Outline each Plasmodium vivax-infected red blood cell.
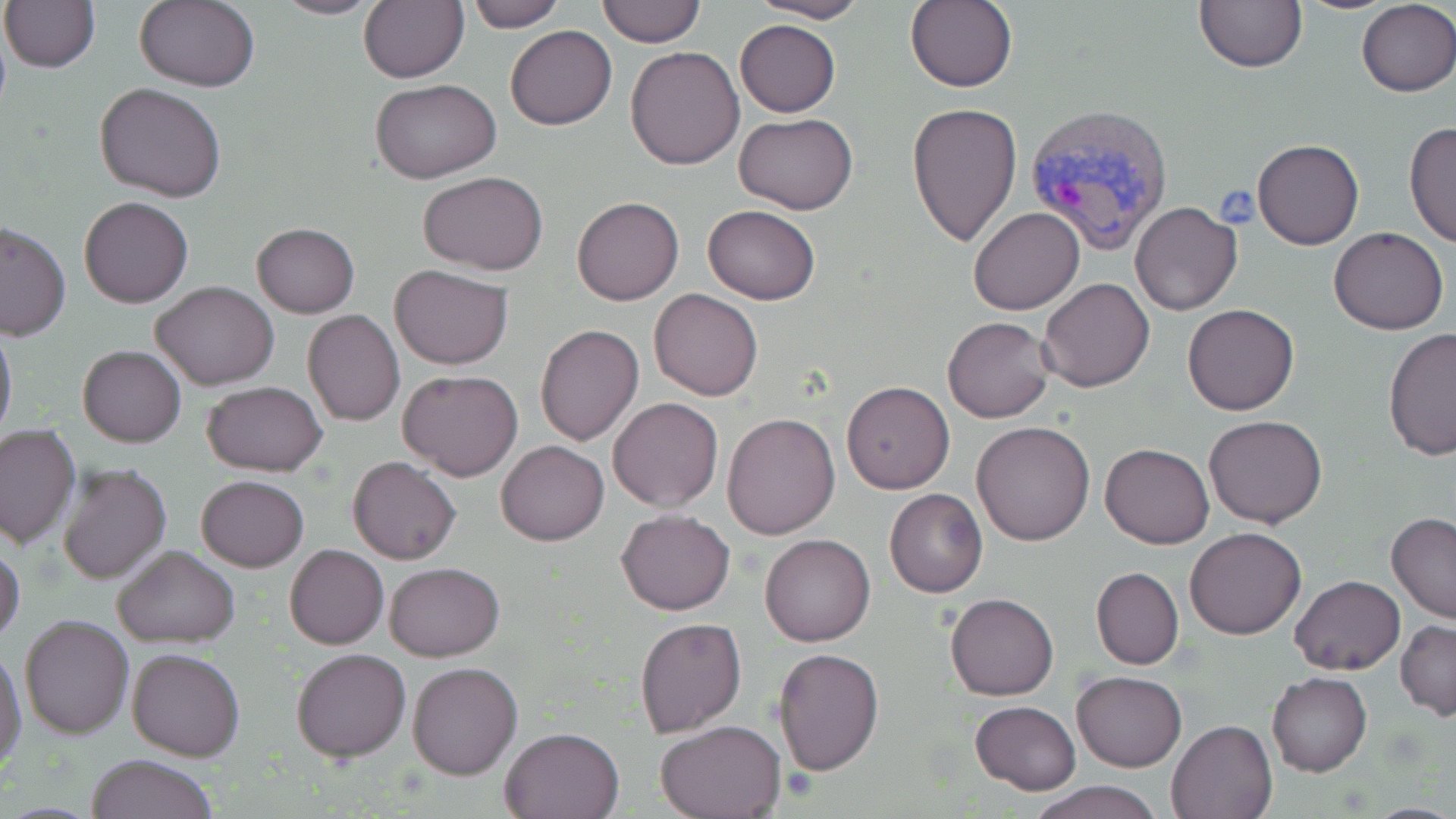

Approximate bounding boxes as (x1, y1, x2, y2) in pixels.
Plasmodium vivax-infected red blood cells: (1023, 102, 1174, 258).

Summary:
  - Platelet locations: (1213, 187, 1261, 229)
  - Uninfected red blood cell locations: (271, 0, 386, 19), (359, 0, 468, 85), (364, 0, 481, 170), (463, 0, 566, 31), (597, 0, 705, 46), (753, 0, 871, 23), (1, 1, 99, 72), (133, 1, 260, 91), (905, 1, 1018, 91), (1194, 1, 1307, 72), (1356, 2, 1456, 95), (734, 19, 840, 117), (504, 26, 616, 130), (626, 45, 746, 170), (371, 79, 502, 184), (95, 83, 226, 203), (907, 102, 1023, 248), (733, 113, 858, 214), (1405, 120, 1456, 252), (1252, 138, 1364, 250), (418, 172, 549, 273), (79, 196, 194, 307), (572, 197, 684, 304), (1130, 201, 1243, 316), (701, 205, 821, 304), (968, 207, 1085, 314), (0, 222, 71, 341), (251, 222, 360, 318), (1329, 227, 1448, 334), (389, 264, 513, 370), (1037, 278, 1155, 392), (151, 281, 279, 389), (650, 289, 762, 401), (1183, 303, 1299, 416), (303, 310, 405, 426), (942, 316, 1055, 423), (0, 322, 17, 449), (534, 324, 644, 446), (1382, 329, 1456, 462), (78, 345, 185, 447), (398, 370, 524, 482), (841, 381, 955, 494), (200, 382, 329, 476), (607, 396, 723, 512), (721, 413, 840, 540), (1203, 415, 1328, 529), (970, 421, 1095, 546), (0, 423, 80, 549), (497, 440, 608, 546), (1100, 443, 1215, 549), (348, 456, 461, 565), (57, 462, 173, 586), (196, 475, 308, 571), (884, 488, 988, 598), (617, 509, 736, 615), (1386, 512, 1456, 624), (1185, 527, 1306, 639), (760, 534, 875, 646), (0, 540, 25, 645), (284, 544, 389, 650), (112, 545, 240, 648), (383, 563, 505, 663), (1091, 567, 1184, 670), (1290, 575, 1404, 675), (945, 592, 1058, 702), (20, 613, 134, 739), (634, 616, 746, 739), (1396, 619, 1456, 720), (127, 645, 245, 762), (0, 647, 26, 778), (291, 648, 411, 762), (773, 648, 884, 776), (408, 661, 523, 779), (1072, 671, 1185, 772), (1267, 674, 1371, 776), (969, 700, 1082, 795), (656, 719, 786, 817), (1167, 719, 1278, 818), (500, 727, 623, 818), (88, 753, 219, 819), (1024, 782, 1169, 819)
  - Slide-level diagnosis: Plasmodium vivax
  - Field of view: single
  - Preparation: thin blood smear
  - Magnification: 1000x
  - Image size: 1456×819 pixels
  - Stain: May-Grünwald-Giemsa
  - Modality: optical microscopy